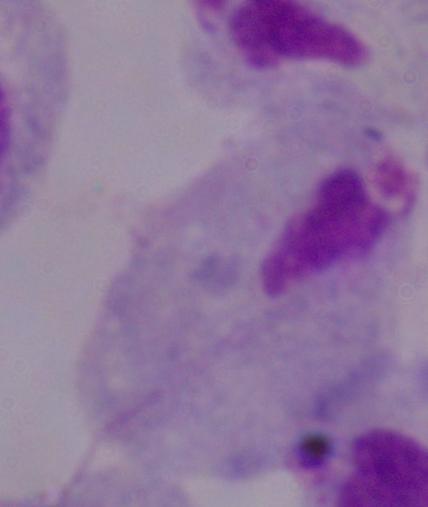
A trichomonad is seen. 1000x magnification. Photomicrograph.